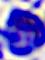

Summary:
  - Modality: micrograph
  - Magnification: 400x
  - Identification: white blood cell